Comment on the morphology of the red blood cells.
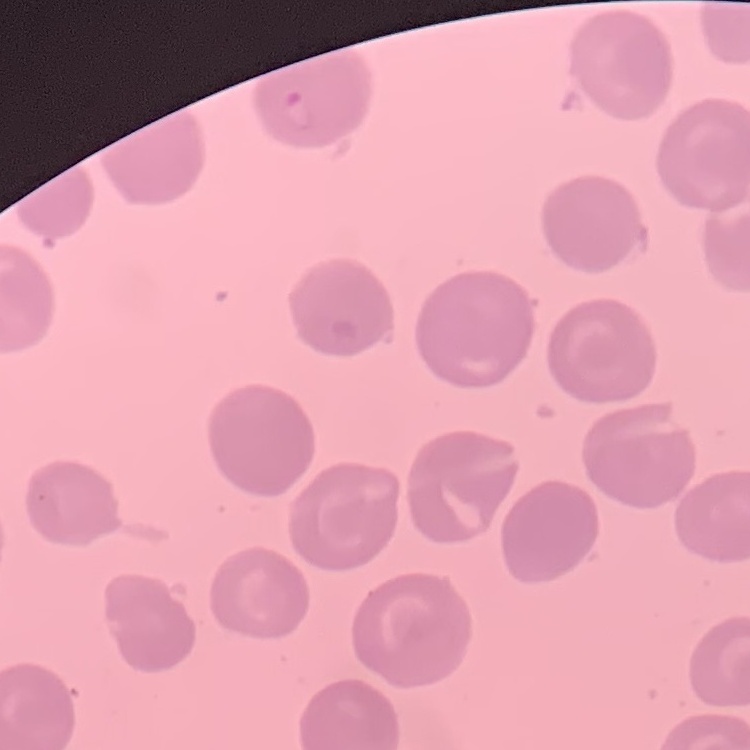
They show no rouleaux formation.

Thin peripheral smear. Stained with either Field's or Giemsa. One tile cut from a larger photomicrograph.